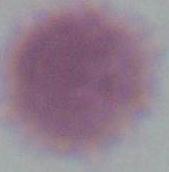
Micrograph. An erythrocyte is shown. 1000x magnification.